Assess the morphology of the red blood cells.
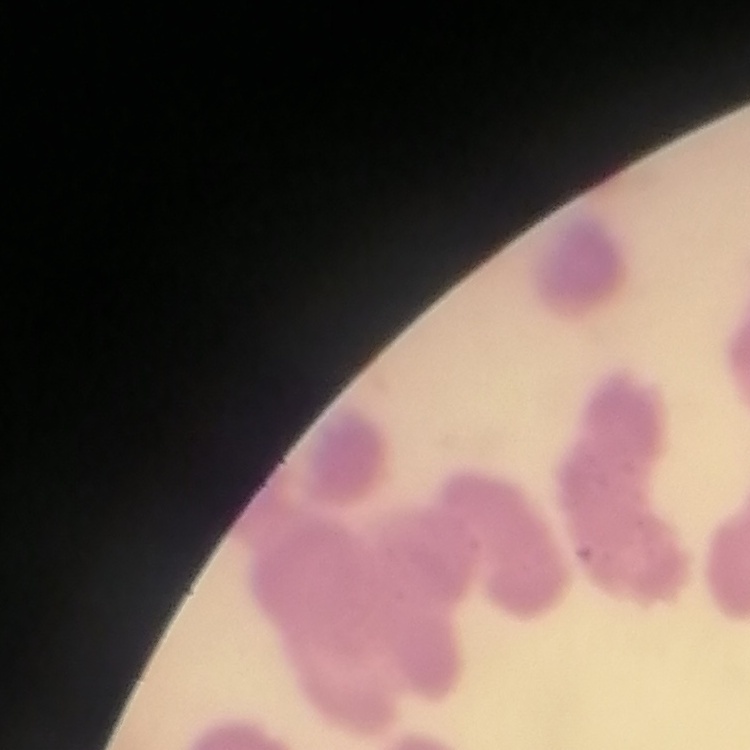

They show rouleaux formation.

Field's or Giemsa stain. Square crop of a larger photomicrograph. Thin blood film.